State the blood parasite species.
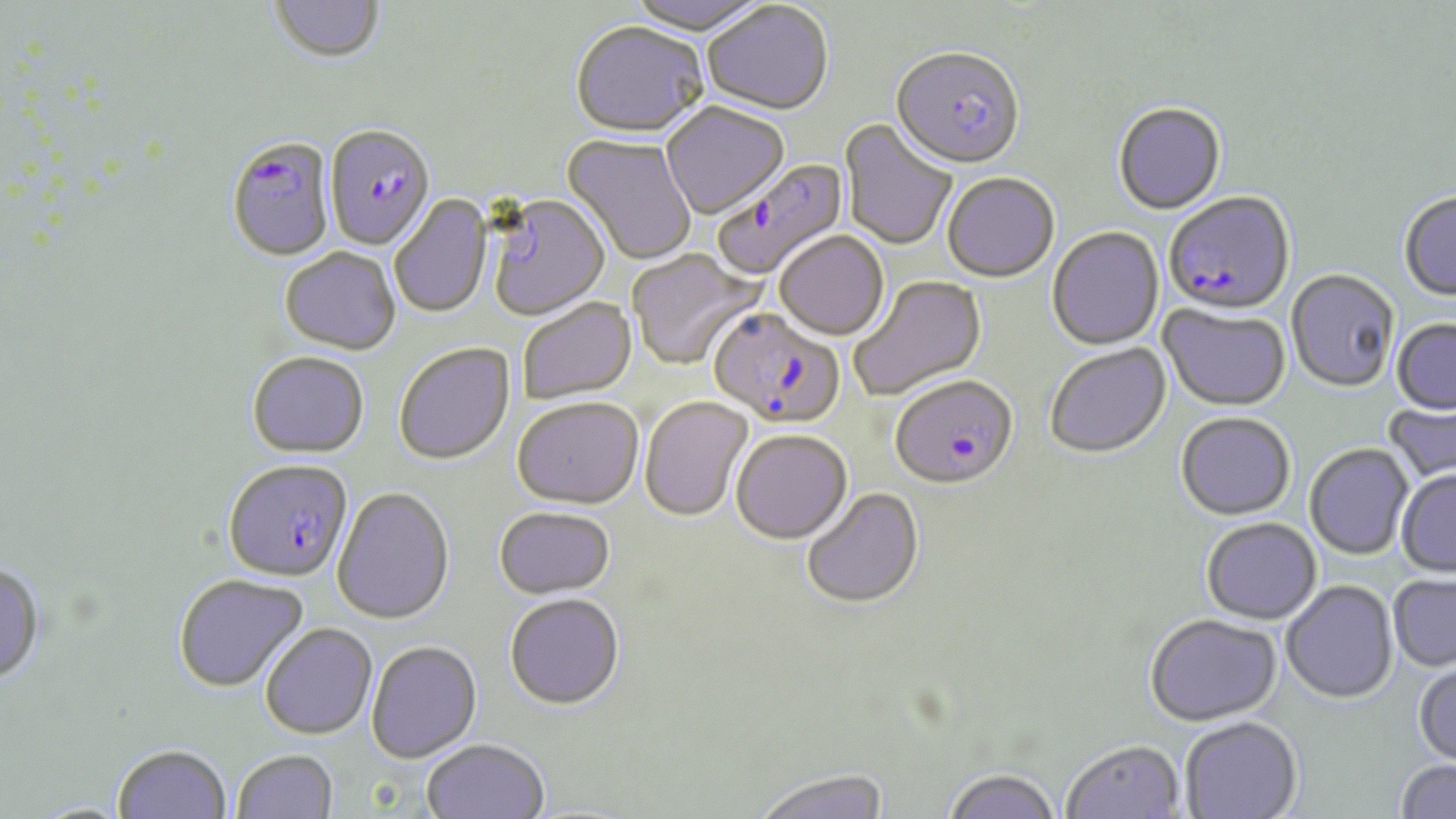
Plasmodium falciparum.

modality: light microscopy
preparation: thin blood film
image_size: 1456×819 pixels
stain: May-Grünwald-Giemsa
magnification: 1000x
plasmodium_falciparum_infected_red_blood_cell_locations: 'approximate bounding boxes as (x1,y1)-(x2,y2) corner pairs in pixels: (890,50)-(1024,173), (326,126)-(434,253), (227,138)-(335,263), (714,159)-(849,281), (1163,195)-(1296,319), (708,309)-(845,431), (890,377)-(1018,492), (224,463)-(352,585)'
field_of_view: single
uninfected_red_blood_cell_locations: 'approximate bounding boxes as (x1,y1)-(x2,y2) corner pairs in pixels: (270,0)-(386,66), (624,0)-(770,38), (702,3)-(833,118), (570,24)-(708,141), (661,104)-(789,221), (1113,105)-(1226,217), (838,119)-(958,252), (561,134)-(697,266), (942,175)-(1059,284), (1399,191)-(1456,301), (389,195)-(492,319), (485,196)-(611,321), (1047,227)-(1164,352), (774,233)-(889,342), (627,249)-(764,371), (280,250)-(401,357), (1286,269)-(1400,392), (849,275)-(988,401), (518,299)-(637,406), (1159,305)-(1291,412), (1392,318)-(1456,414), (394,344)-(515,466), (1044,345)-(1171,461), (247,354)-(369,460), (639,397)-(753,524), (1383,400)-(1456,486), (512,401)-(643,512), (1175,413)-(1296,521), (731,432)-(853,547), (1304,443)-(1414,560), (1397,470)-(1456,577), (332,489)-(455,627), (802,489)-(925,611), (494,509)-(615,602), (1201,517)-(1321,625), (0,564)-(46,687), (1388,572)-(1456,671), (173,575)-(309,693), (1281,580)-(1398,703), (504,596)-(625,712), (1144,614)-(1282,727), (261,625)-(378,741), (366,643)-(482,765), (1413,660)-(1456,768), (1180,717)-(1303,819), (422,740)-(549,819), (1061,742)-(1187,819), (113,744)-(232,819), (233,751)-(339,819), (1395,759)-(1456,818), (751,769)-(891,819), (941,770)-(1063,819)'